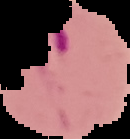
From a thin blood smear. Result: Plasmodium parasites identified. Cell region segmented out of the field of view; the surrounding area is masked to black. Image is 130×139 pixels.